Give the position of every leukocyte visible.
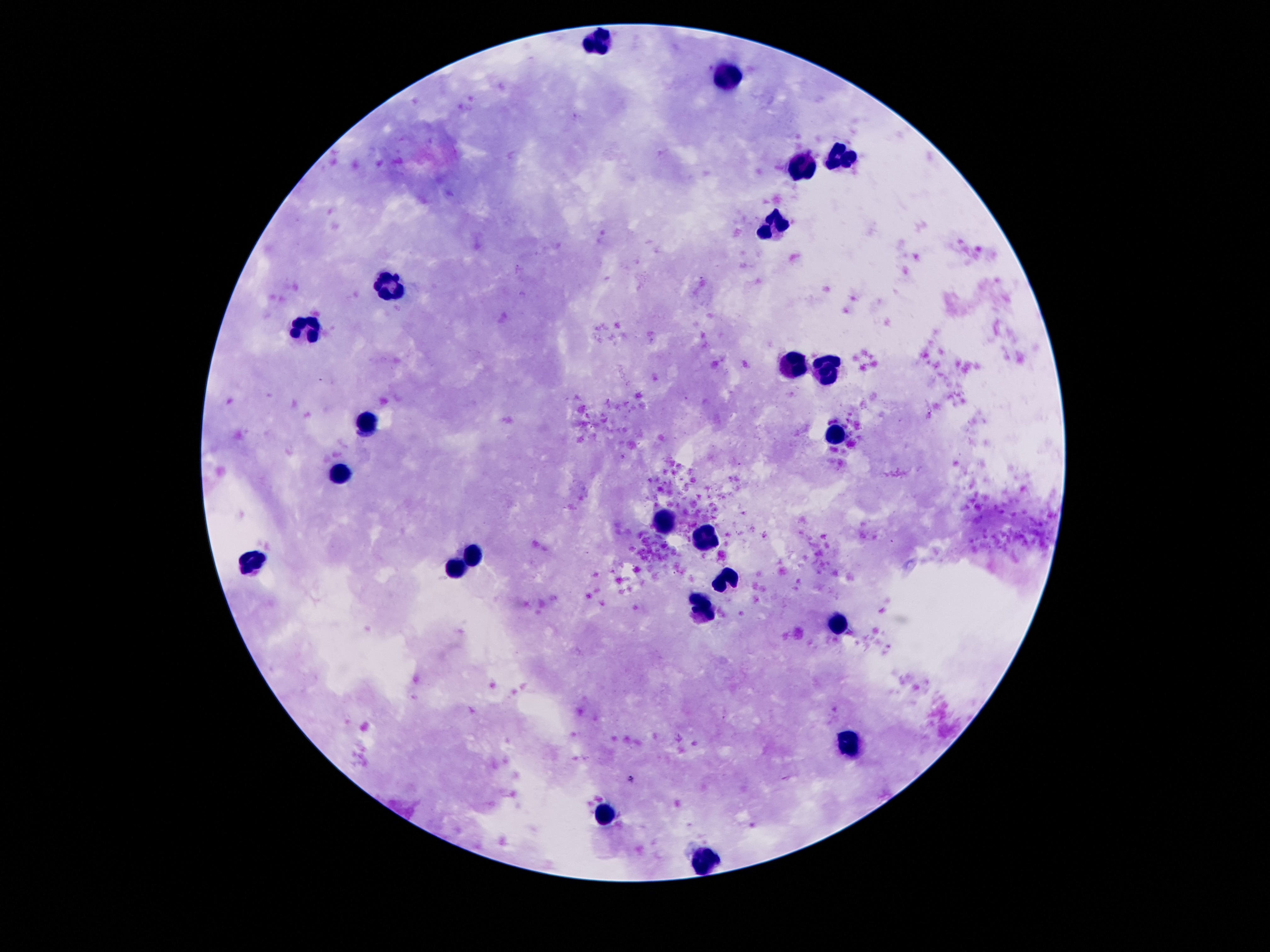
Approximate centers as [x, y] in pixels.
Leukocytes: [598, 44], [724, 72], [839, 158], [804, 169], [774, 229], [392, 282], [308, 328], [791, 363], [827, 370], [367, 427], [837, 435], [337, 474], [663, 525], [705, 538], [472, 553], [251, 562], [455, 567], [726, 577], [703, 609], [837, 623], [850, 745], [604, 812], [707, 861].

{
  "capture": "smartphone camera through the microscope eyepiece",
  "patient_malaria_status": "negative",
  "preparation": "thick peripheral-blood smear",
  "field_of_view": "one from this slide",
  "stain": "Giemsa",
  "image_size": "1270×952 pixels",
  "magnification": "100x"
}